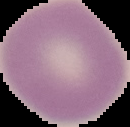

image type = cell region segmented out of the field of view; surrounding area masked to black
image size = 130×127 pixels
malaria status = uninfected
preparation = thin blood film